Outline each blood parasite and name the species.
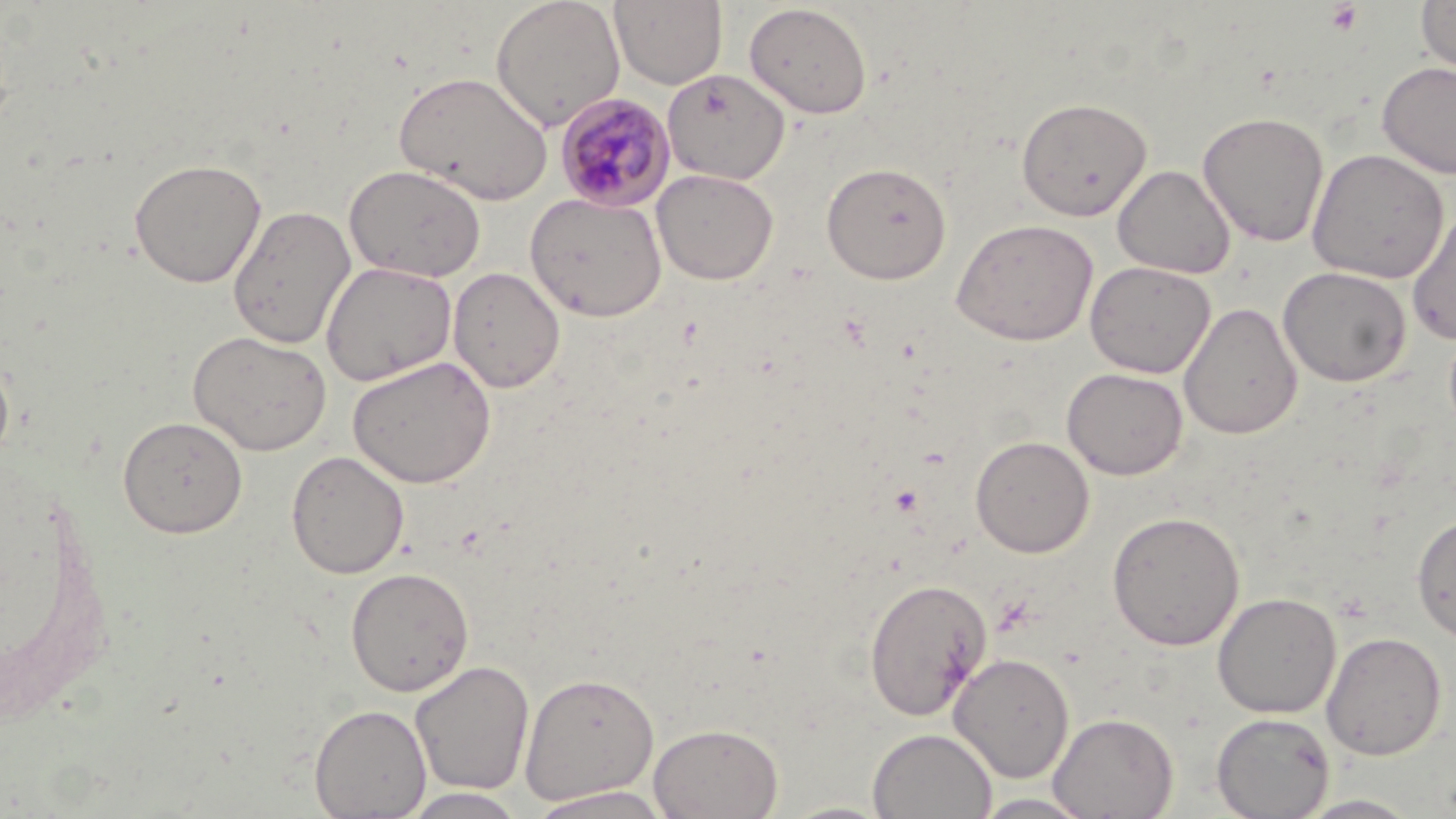

Approximate bounding boxes as named x1/y1/x2/y2 corners in pixels.
Plasmodium malariae-infected red blood cells: (x1=554, y1=93, x2=675, y2=212).
No Plasmodium falciparum, Plasmodium ovale, Plasmodium vivax, Babesia divergens, or Trypanosoma brucei observed.

Uninfected red blood cell locations: (x1=490, y1=0, x2=626, y2=132), (x1=610, y1=0, x2=727, y2=89), (x1=1416, y1=0, x2=1456, y2=75), (x1=744, y1=3, x2=872, y2=119), (x1=1376, y1=61, x2=1456, y2=179), (x1=661, y1=69, x2=790, y2=185), (x1=394, y1=71, x2=553, y2=206), (x1=1016, y1=96, x2=1153, y2=221), (x1=1197, y1=110, x2=1330, y2=247), (x1=1306, y1=148, x2=1449, y2=284), (x1=129, y1=157, x2=267, y2=288), (x1=821, y1=161, x2=952, y2=284), (x1=343, y1=163, x2=487, y2=283), (x1=1113, y1=164, x2=1236, y2=279), (x1=652, y1=168, x2=779, y2=285), (x1=525, y1=192, x2=667, y2=322), (x1=1406, y1=205, x2=1456, y2=345), (x1=227, y1=206, x2=356, y2=349), (x1=951, y1=218, x2=1099, y2=346), (x1=1084, y1=260, x2=1215, y2=379), (x1=320, y1=261, x2=457, y2=386), (x1=1277, y1=266, x2=1412, y2=387), (x1=449, y1=267, x2=565, y2=393), (x1=1179, y1=302, x2=1303, y2=439), (x1=188, y1=330, x2=332, y2=456), (x1=0, y1=348, x2=15, y2=467), (x1=348, y1=355, x2=497, y2=489), (x1=1062, y1=367, x2=1188, y2=480), (x1=117, y1=415, x2=248, y2=538), (x1=970, y1=435, x2=1094, y2=557), (x1=286, y1=450, x2=410, y2=579), (x1=1107, y1=510, x2=1245, y2=650), (x1=1411, y1=512, x2=1455, y2=642), (x1=345, y1=566, x2=475, y2=696), (x1=863, y1=577, x2=991, y2=722), (x1=1212, y1=592, x2=1341, y2=719), (x1=1321, y1=631, x2=1447, y2=760), (x1=948, y1=652, x2=1075, y2=783), (x1=410, y1=660, x2=535, y2=796), (x1=519, y1=671, x2=660, y2=804), (x1=309, y1=704, x2=432, y2=818), (x1=1048, y1=712, x2=1178, y2=819), (x1=1211, y1=712, x2=1334, y2=819), (x1=648, y1=721, x2=784, y2=819), (x1=868, y1=728, x2=997, y2=819), (x1=525, y1=786, x2=676, y2=818), (x1=401, y1=788, x2=528, y2=818), (x1=971, y1=792, x2=1098, y2=818), (x1=1294, y1=793, x2=1424, y2=818), (x1=774, y1=800, x2=896, y2=818). Platelet locations: (x1=1325, y1=2, x2=1364, y2=35). Slide-level diagnosis: Plasmodium malariae. Captured at 1000x magnification. May-Grünwald-Giemsa stain. One field of a larger specimen. Thin blood smear. Optical microscopy. Image is 1456×819 pixels.